Name the parasite shown.
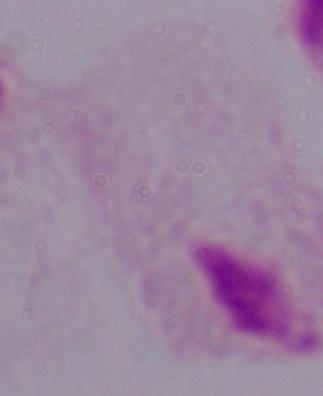

A trichomonad.

Summary:
  - Modality: micrograph
  - Magnification: 1000x